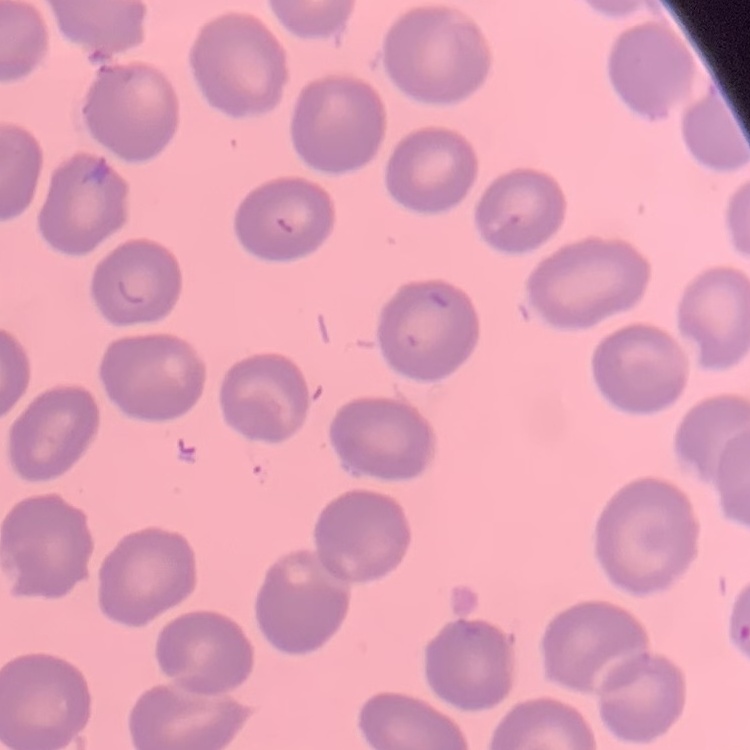
Summary:
  - Red blood cell morphology: no rouleaux formation
  - Image type: square crop of a larger photomicrograph
  - Preparation: thin peripheral smear
  - Stain: Field's or Giemsa